Give the position of every Plasmodium parasite.
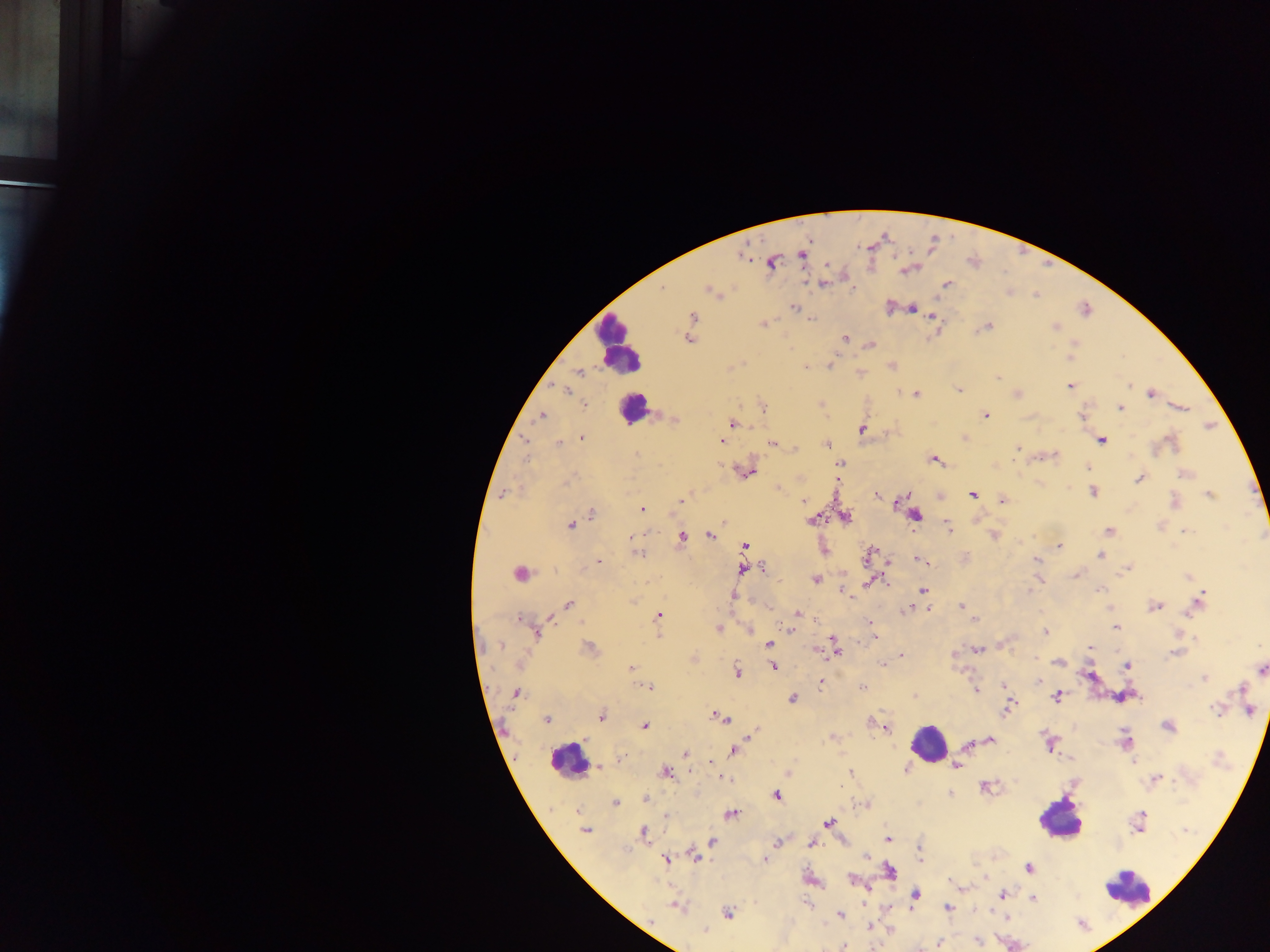
Approximate centers as {x, y} in pixels.
Plasmodium parasites: {903, 271}, {819, 282}, {794, 307}, {912, 309}, {934, 315}, {694, 317}, {764, 323}, {990, 327}, {1055, 328}, {692, 330}, {689, 338}, {845, 338}, {871, 344}, {830, 363}, {893, 366}, {804, 367}, {576, 374}, {997, 377}, {1069, 385}, {565, 391}, {957, 391}, {1151, 392}, {917, 393}, {583, 405}, {1120, 407}, {1181, 407}, {539, 416}, {987, 416}, {733, 422}, {862, 429}, {582, 439}, {721, 439}, {965, 439}, {1101, 440}, {526, 441}, {557, 442}, {772, 443}, {828, 445}, {795, 446}, {1020, 448}, {1016, 450}, {637, 454}, {1055, 456}, {527, 458}, {934, 460}, {744, 470}, {569, 479}, {1138, 479}, {837, 482}, {780, 488}, {1092, 492}, {505, 493}, {908, 494}, {972, 495}, {877, 496}, {1210, 496}, {682, 499}, {1002, 500}, {802, 501}, {899, 501}, {642, 509}, {591, 514}, {570, 526}, {949, 528}, {1111, 530}, {1184, 530}, {708, 534}, {681, 535}, {993, 535}, {1060, 546}, {639, 553}, {1100, 554}, {598, 560}, {1036, 560}, {764, 566}, {517, 574}, {1075, 574}, {1187, 577}, {816, 579}, {1030, 587}, {1100, 590}, {923, 591}, {1028, 591}, {1203, 593}, {734, 594}, {568, 605}, {1157, 606}, {960, 607}, {1107, 607}, {904, 609}, {928, 609}, {796, 612}, {1190, 613}, {658, 614}, {975, 617}, {520, 618}, {1115, 628}, {720, 629}, {790, 630}, {1043, 631}, {1177, 631}, {832, 639}, {505, 643}, {768, 643}, {835, 644}, {501, 646}, {590, 646}, {978, 648}, {1090, 649}, {1177, 653}, {955, 655}, {1034, 657}, {1058, 663}, {522, 664}, {1126, 665}, {773, 667}, {631, 668}, {738, 670}, {1260, 670}, {1202, 677}, {1037, 680}, {821, 683}, {649, 686}, {1004, 686}, {862, 687}, {1241, 688}, {977, 690}, {516, 693}, {914, 695}, {792, 697}, {1056, 697}, {1011, 705}, {1214, 710}, {1006, 711}, {601, 715}, {716, 716}, {722, 719}, {547, 720}, {871, 722}, {644, 723}, {886, 726}, {753, 732}, {827, 738}, {990, 739}, {968, 746}, {734, 750}, {686, 753}, {1134, 761}, {911, 762}, {710, 763}, {957, 766}, {666, 772}, {850, 774}, {724, 777}, {1158, 777}, {841, 788}, {986, 788}, {950, 793}, {776, 797}, {645, 798}, {615, 804}, {578, 811}, {731, 814}, {1143, 814}, {829, 822}, {587, 831}, {642, 832}, {888, 838}, {811, 842}, {710, 843}, {779, 843}, {696, 856}, {866, 857}, {666, 860}, {765, 860}, {1027, 868}, {853, 879}, {916, 893}, {1003, 895}, {1033, 898}, {674, 906}, {946, 907}, {728, 913}, {840, 915}, {869, 925}, {706, 930}, {977, 941}, {939, 942}, {844, 945}.

Leukocyte locations: {623, 341}, {635, 412}, {927, 741}, {562, 761}, {1054, 822}, {1129, 894}. Sample from Ghana. Thick blood film. Image is 1270×952 pixels. One field of view. Mobile-phone photograph taken through the microscope.